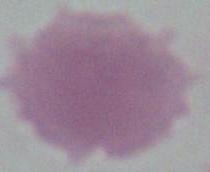 Captured at 1000x magnification. A red blood cell is shown. Photomicrograph.